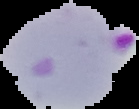
image_type: cell region segmented out of the field of view; surrounding area masked to black
malaria_status: parasitized
image_size: 139×109 pixels
preparation: thin blood film